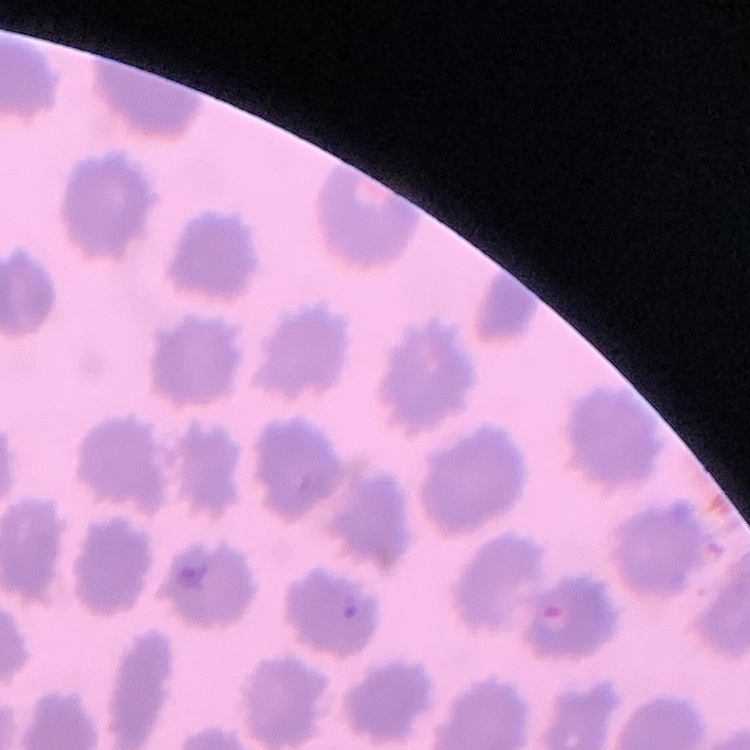

Summary:
  - Erythrocyte morphology: no rouleaux formation
  - Image type: one tile cut from a larger photomicrograph
  - Preparation: thin peripheral smear
  - Stain: Field's or Giemsa